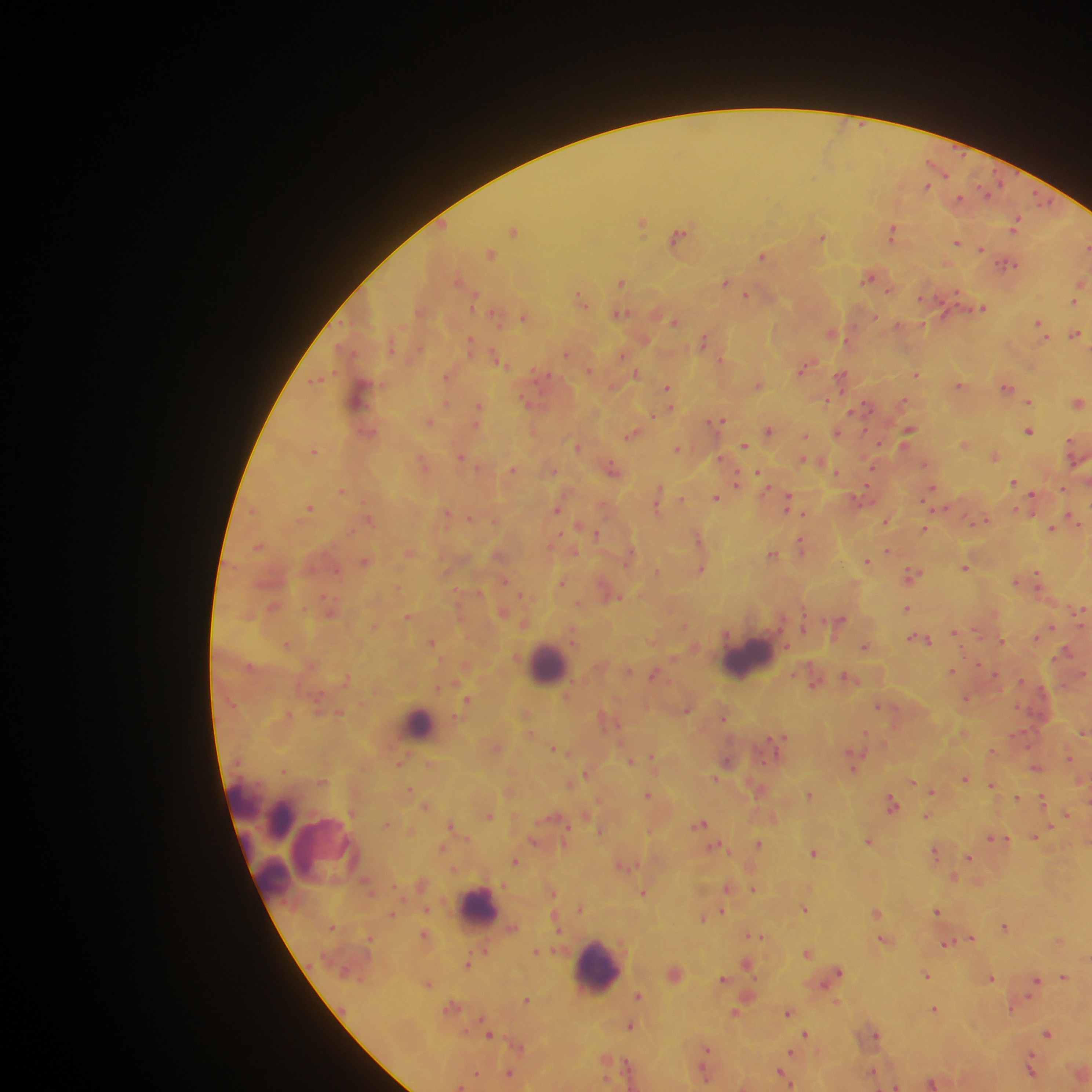
malaria parasite locations = approximate centers as {x, y} in pixels: {927, 186}, {959, 198}, {1042, 201}, {642, 222}, {1016, 222}, {514, 230}, {893, 231}, {678, 236}, {822, 238}, {956, 242}, {982, 248}, {491, 253}, {762, 257}, {1008, 264}, {867, 278}, {725, 281}, {621, 282}, {890, 291}, {957, 294}, {745, 295}, {580, 299}, {1074, 301}, {983, 309}, {620, 313}, {524, 316}, {674, 320}, {1038, 323}, {831, 333}, {1074, 334}, {703, 340}, {470, 342}, {566, 353}, {498, 359}, {804, 367}, {636, 372}, {916, 373}, {841, 375}, {318, 380}, {960, 385}, {758, 386}, {668, 387}, {1006, 387}, {825, 400}, {1029, 401}, {1078, 402}, {864, 406}, {478, 407}, {654, 415}, {720, 419}, {430, 421}, {769, 430}, {909, 430}, {1029, 431}, {838, 432}, {631, 435}, {805, 435}, {964, 444}, {744, 445}, {578, 447}, {1073, 448}, {677, 449}, {314, 451}, {994, 456}, {461, 457}, {805, 461}, {873, 468}, {512, 469}, {612, 469}, {551, 470}, {758, 472}, {836, 472}, {736, 482}, {1014, 483}, {1063, 488}, {931, 490}, {342, 491}, {659, 491}, {716, 497}, {861, 498}, {1031, 499}, {682, 500}, {787, 502}, {656, 506}, {309, 508}, {557, 508}, {447, 513}, {804, 513}, {469, 518}, {1074, 518}, {369, 519}, {886, 521}, {982, 521}, {924, 528}, {1051, 529}, {595, 533}, {698, 538}, {801, 546}, {259, 547}, {888, 551}, {409, 552}, {773, 554}, {365, 561}, {866, 561}, {965, 567}, {701, 569}, {657, 571}, {912, 574}, {1037, 579}, {505, 581}, {1016, 581}, {561, 582}, {521, 595}, {615, 596}, {907, 607}, {1079, 610}, {408, 616}, {839, 620}, {803, 629}, {956, 632}, {921, 639}, {1000, 640}, {431, 642}, {864, 646}, {1067, 652}, {952, 671}, {653, 675}, {995, 675}, {848, 677}, {813, 682}, {966, 698}, {467, 699}, {878, 705}, {687, 709}, {723, 715}, {1083, 732}, {780, 740}, {554, 749}, {1070, 758}, {652, 759}, {728, 760}, {631, 761}, {400, 762}, {853, 767}, {1035, 767}, {587, 773}, {715, 778}, {965, 778}, {914, 782}, {991, 785}, {410, 789}, {931, 792}, {809, 794}, {648, 795}, {1017, 798}, {1042, 800}, {892, 805}, {1066, 814}, {490, 815}, {927, 816}, {386, 823}, {451, 824}, {701, 824}, {601, 830}, {1036, 836}, {993, 838}, {533, 839}, {869, 840}, {758, 843}, {714, 847}, {935, 852}, {813, 853}, {969, 857}, {515, 861}, {954, 879}, {727, 888}, {753, 889}, {644, 893}, {805, 908}, {580, 909}, {723, 911}, {936, 911}, {875, 912}, {703, 918}, {1004, 926}, {756, 936}, {970, 939}, {882, 940}, {947, 943}, {484, 950}, {537, 951}, {807, 952}, {467, 963}, {746, 964}, {838, 972}, {926, 975}, {1064, 976}, {990, 977}, {723, 979}, {1036, 981}, {428, 984}, {638, 996}, {527, 999}, {1011, 1008}, {934, 1009}, {735, 1013}, {788, 1013}, {630, 1026}, {874, 1033}, {1047, 1033}, {806, 1034}, {489, 1035}, {707, 1049}, {791, 1053}, {1031, 1068}, {705, 1071}, {873, 1072}, {477, 1073}, {510, 1073}, {784, 1075}, {933, 1083}, {895, 1086}
field of view = single
country = Ghana
image size = 1092×1092 pixels
capture = mobile-phone photograph through a microscope
leukocyte locations = approximate centers as {x, y} in pixels: {747, 658}, {547, 661}, {418, 724}, {247, 800}, {283, 818}, {329, 844}, {272, 879}, {480, 906}, {596, 967}
preparation = thick blood smear